Name the parasite shown.
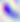
Toxoplasma gondii.

Summary:
  - Modality: photomicrograph
  - Magnification: 400x